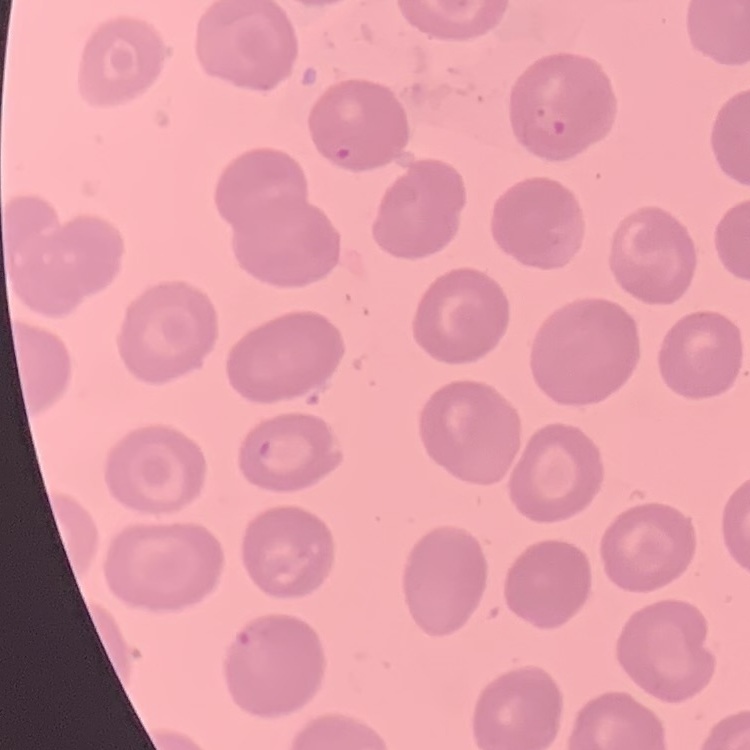 The red blood cells exhibit no rouleaux formation. Stained with either Field's or Giemsa. Thin blood smear. One tile cut from a larger photomicrograph.